State which parasite is depicted.
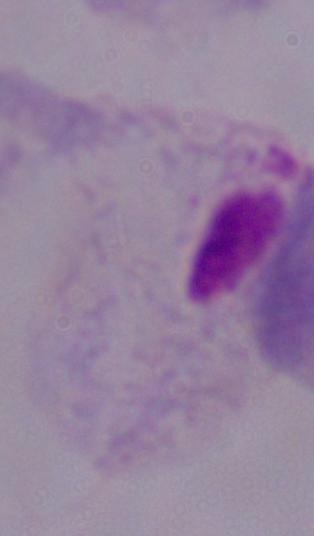
This is a trichomonad.

Summary:
  - Modality: photomicrograph
  - Magnification: 1000x